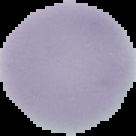
Image is 136×136 pixels. Segmented cell region on a black background. From a thin blood smear. Malaria status: uninfected.